Name the cell type shown.
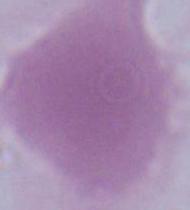
This is an erythrocyte.

1000x magnification. Photomicrograph.